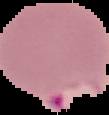
{
  "image_size": "109×115 pixels",
  "image_type": "segmented cell region with the area outside set to black",
  "preparation": "thin blood smear",
  "result": "malaria parasites identified"
}